Assess the morphology of the erythrocytes.
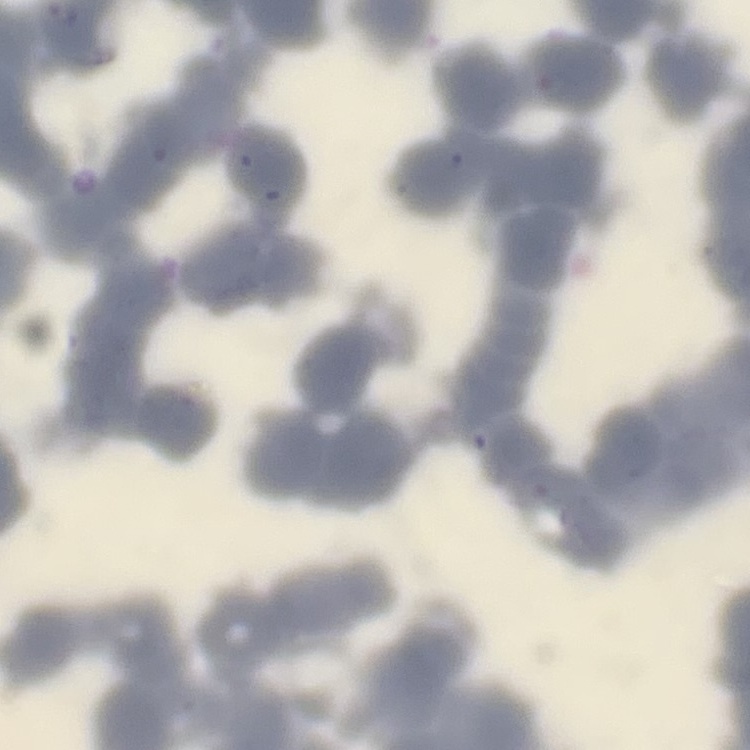

They show rouleaux formation.

stain = Field's or Giemsa
image type = one tile cut from a larger photomicrograph
preparation = thin blood film